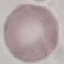

Result: no malaria parasites detected. Acquired by smartphone through the microscope eyepiece. Thin blood smear. Cell patch, automatically extracted from a larger field of view and resized to 64 × 64 pixels. Giemsa-stained preparation.